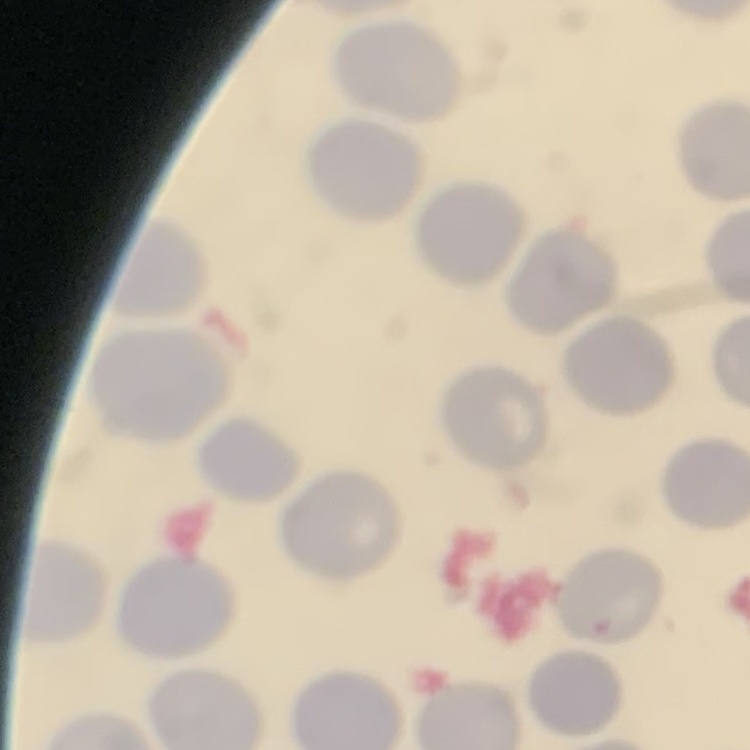

The red blood cells exhibit no rouleaux formation. Thin blood smear. Square crop of a larger photomicrograph. Stained with either Field's or Giemsa.